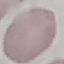

Summary:
  - Malaria status: uninfected
  - Preparation: thin blood film
  - Capture: smartphone camera at the microscope eyepiece
  - Stain: Giemsa
  - Image type: cell patch, automatically extracted from a larger field of view and resized to 64 × 64 pixels